Assess this cell for malaria.
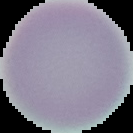

It is uninfected.

Summary:
  - Preparation: thin blood film
  - Image type: segmented cell region on a black background
  - Image size: 133×133 pixels